Assess the morphology of the erythrocytes.
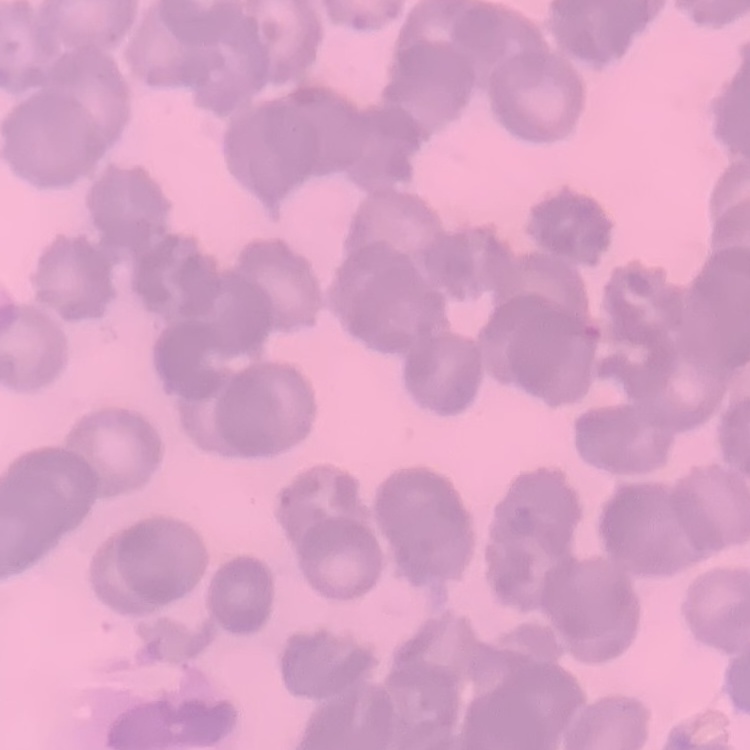
Rouleaux formation.

Summary:
  - Preparation: thin blood film
  - Image type: one tile cut from a larger photomicrograph
  - Stain: Field's or Giemsa